Point out each malaria parasite.
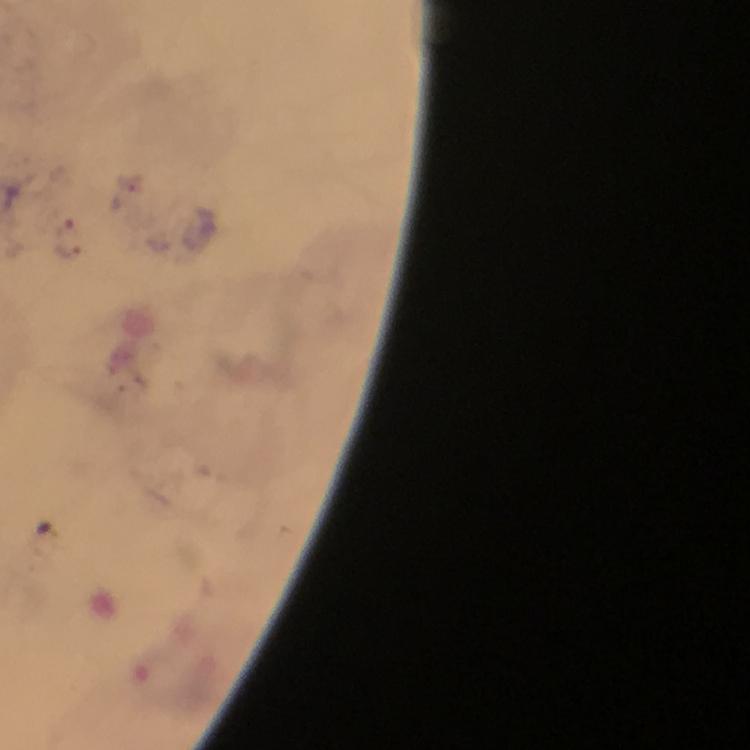
Approximate object centers, in pixels from the top-left corner.
Malaria parasites: (x=68, y=238).

Cropped region of a single field of view. From a diagnostic examination for malaria. Thick smear. At 100x magnification. Image is 750×750 pixels. Giemsa stain. Immersion oil applied. Smartphone photograph taken through a microscope.